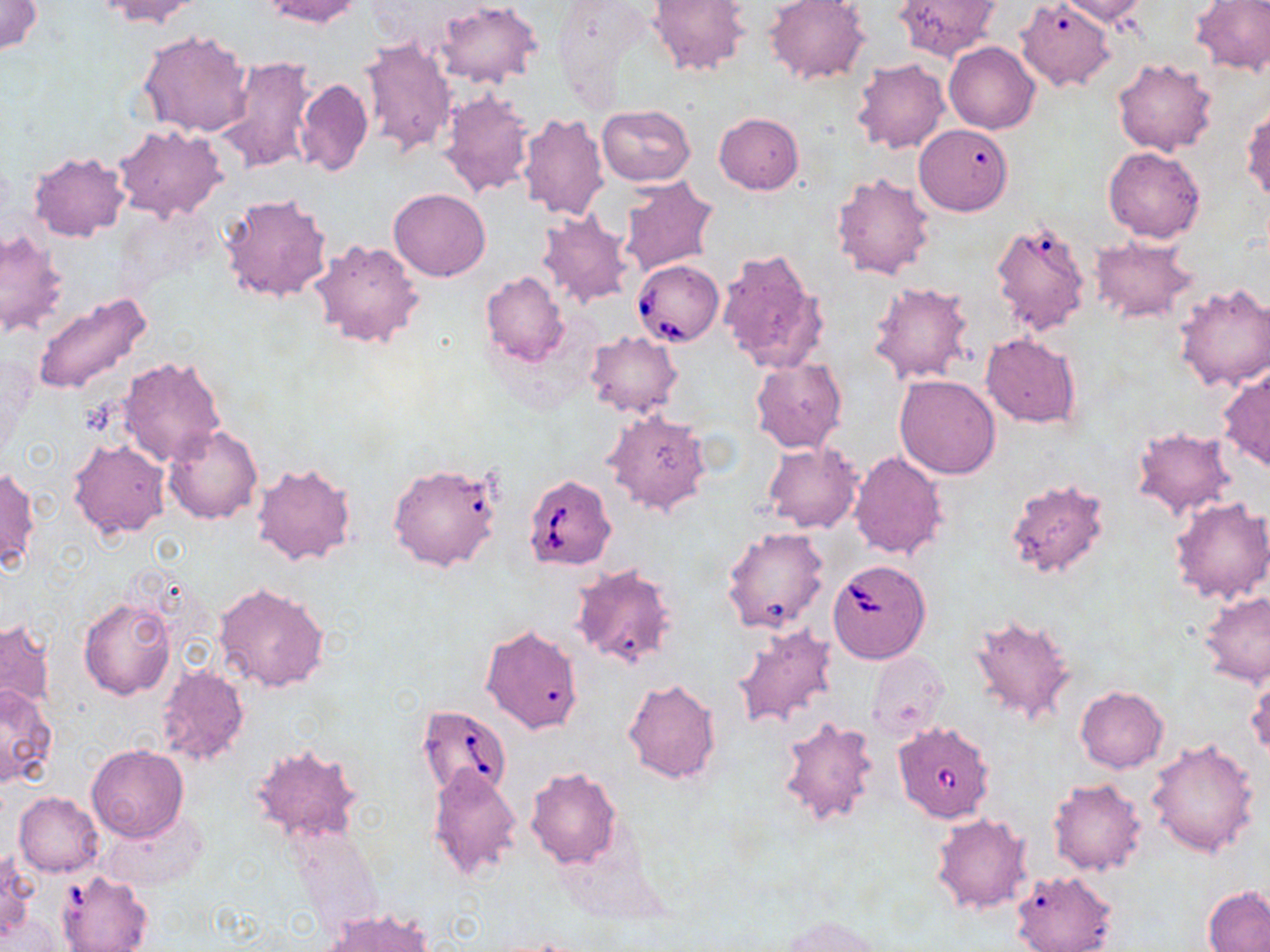
Approximate bounding boxes as named x1/y1/x2/y2 corners in pixels. Uninfected red blood cell locations: (x1=0, y1=0, x2=43, y2=56), (x1=92, y1=0, x2=203, y2=27), (x1=260, y1=0, x2=364, y2=27), (x1=554, y1=0, x2=660, y2=106), (x1=647, y1=0, x2=748, y2=77), (x1=893, y1=0, x2=1000, y2=62), (x1=1017, y1=0, x2=1115, y2=91), (x1=1056, y1=0, x2=1149, y2=25), (x1=1191, y1=0, x2=1270, y2=76), (x1=764, y1=1, x2=871, y2=85), (x1=434, y1=3, x2=541, y2=87), (x1=137, y1=29, x2=254, y2=139), (x1=357, y1=37, x2=457, y2=159), (x1=944, y1=41, x2=1040, y2=134), (x1=213, y1=56, x2=318, y2=176), (x1=1112, y1=57, x2=1218, y2=156), (x1=852, y1=58, x2=950, y2=154), (x1=295, y1=77, x2=373, y2=177), (x1=436, y1=87, x2=536, y2=198), (x1=596, y1=105, x2=696, y2=186), (x1=1243, y1=107, x2=1270, y2=203), (x1=516, y1=112, x2=608, y2=221), (x1=713, y1=113, x2=803, y2=194), (x1=914, y1=123, x2=1013, y2=215), (x1=113, y1=124, x2=227, y2=221), (x1=1104, y1=147, x2=1205, y2=242), (x1=28, y1=150, x2=130, y2=242), (x1=831, y1=173, x2=935, y2=280), (x1=617, y1=176, x2=720, y2=276), (x1=389, y1=187, x2=491, y2=281), (x1=219, y1=192, x2=334, y2=303), (x1=535, y1=210, x2=634, y2=310), (x1=994, y1=217, x2=1092, y2=338), (x1=1, y1=228, x2=68, y2=340), (x1=1089, y1=236, x2=1198, y2=325), (x1=308, y1=239, x2=427, y2=350), (x1=717, y1=247, x2=829, y2=374), (x1=480, y1=271, x2=569, y2=367), (x1=867, y1=279, x2=975, y2=386), (x1=1173, y1=283, x2=1270, y2=393), (x1=31, y1=290, x2=154, y2=398), (x1=583, y1=331, x2=682, y2=418), (x1=981, y1=333, x2=1081, y2=427), (x1=117, y1=356, x2=226, y2=467), (x1=751, y1=358, x2=847, y2=454), (x1=1218, y1=365, x2=1270, y2=475), (x1=894, y1=374, x2=1001, y2=478), (x1=603, y1=407, x2=714, y2=516), (x1=164, y1=424, x2=262, y2=524), (x1=1129, y1=427, x2=1238, y2=519), (x1=69, y1=438, x2=172, y2=538), (x1=762, y1=443, x2=863, y2=533), (x1=847, y1=450, x2=947, y2=558), (x1=251, y1=461, x2=358, y2=567), (x1=389, y1=461, x2=502, y2=573), (x1=0, y1=466, x2=38, y2=570), (x1=1003, y1=479, x2=1112, y2=582), (x1=1168, y1=496, x2=1269, y2=605), (x1=722, y1=525, x2=828, y2=635), (x1=571, y1=563, x2=679, y2=671), (x1=213, y1=581, x2=331, y2=692), (x1=1199, y1=592, x2=1270, y2=687), (x1=80, y1=597, x2=174, y2=699), (x1=968, y1=612, x2=1080, y2=730), (x1=0, y1=619, x2=54, y2=713), (x1=733, y1=623, x2=839, y2=731), (x1=482, y1=625, x2=584, y2=733), (x1=867, y1=650, x2=952, y2=738), (x1=153, y1=663, x2=250, y2=768), (x1=1246, y1=666, x2=1269, y2=761), (x1=623, y1=678, x2=722, y2=784), (x1=0, y1=685, x2=57, y2=789), (x1=1075, y1=686, x2=1169, y2=773), (x1=777, y1=714, x2=882, y2=830), (x1=1145, y1=739, x2=1261, y2=859), (x1=249, y1=744, x2=363, y2=842), (x1=86, y1=745, x2=188, y2=843), (x1=427, y1=767, x2=521, y2=882), (x1=525, y1=767, x2=623, y2=869), (x1=1047, y1=777, x2=1147, y2=875), (x1=14, y1=792, x2=103, y2=878), (x1=98, y1=809, x2=209, y2=893), (x1=931, y1=813, x2=1033, y2=915), (x1=1, y1=851, x2=38, y2=943), (x1=1011, y1=870, x2=1117, y2=952), (x1=60, y1=872, x2=149, y2=951), (x1=1204, y1=886, x2=1270, y2=952), (x1=322, y1=909, x2=433, y2=951), (x1=782, y1=915, x2=883, y2=952). Babesia divergens-infected red blood cell locations: (x1=632, y1=258, x2=725, y2=346), (x1=522, y1=474, x2=616, y2=570), (x1=827, y1=558, x2=931, y2=663), (x1=415, y1=703, x2=512, y2=800), (x1=893, y1=721, x2=996, y2=823). Slide-level diagnosis: Babesia divergens. Image is 1270×952 pixels. May-Grünwald-Giemsa-stained preparation. Single field of view. Captured at 1000x magnification. Light microscopy. Thin blood film.